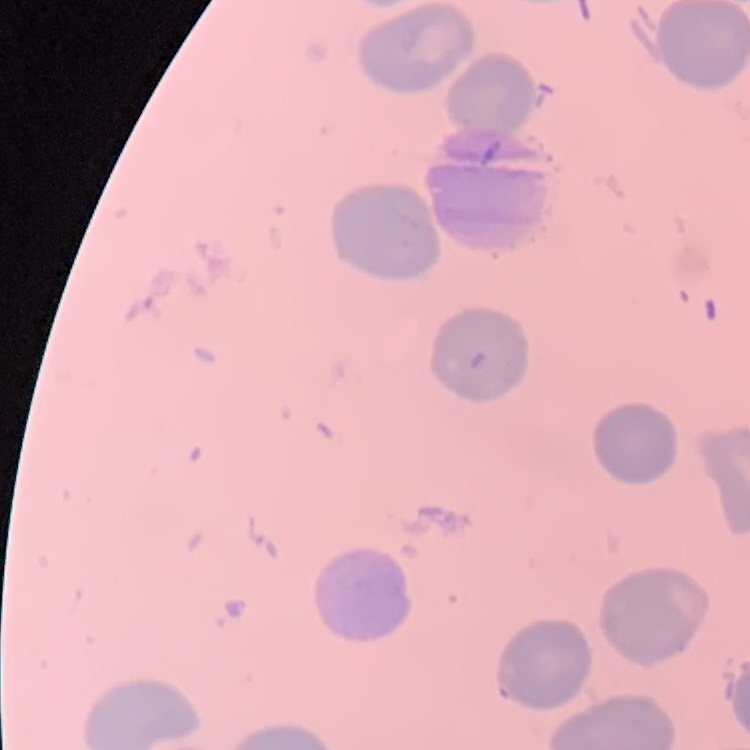 The erythrocytes exhibit no rouleaux formation. Thin blood film. Stained with either Field's or Giemsa. Square crop of a larger photomicrograph.